Name the blood parasite species.
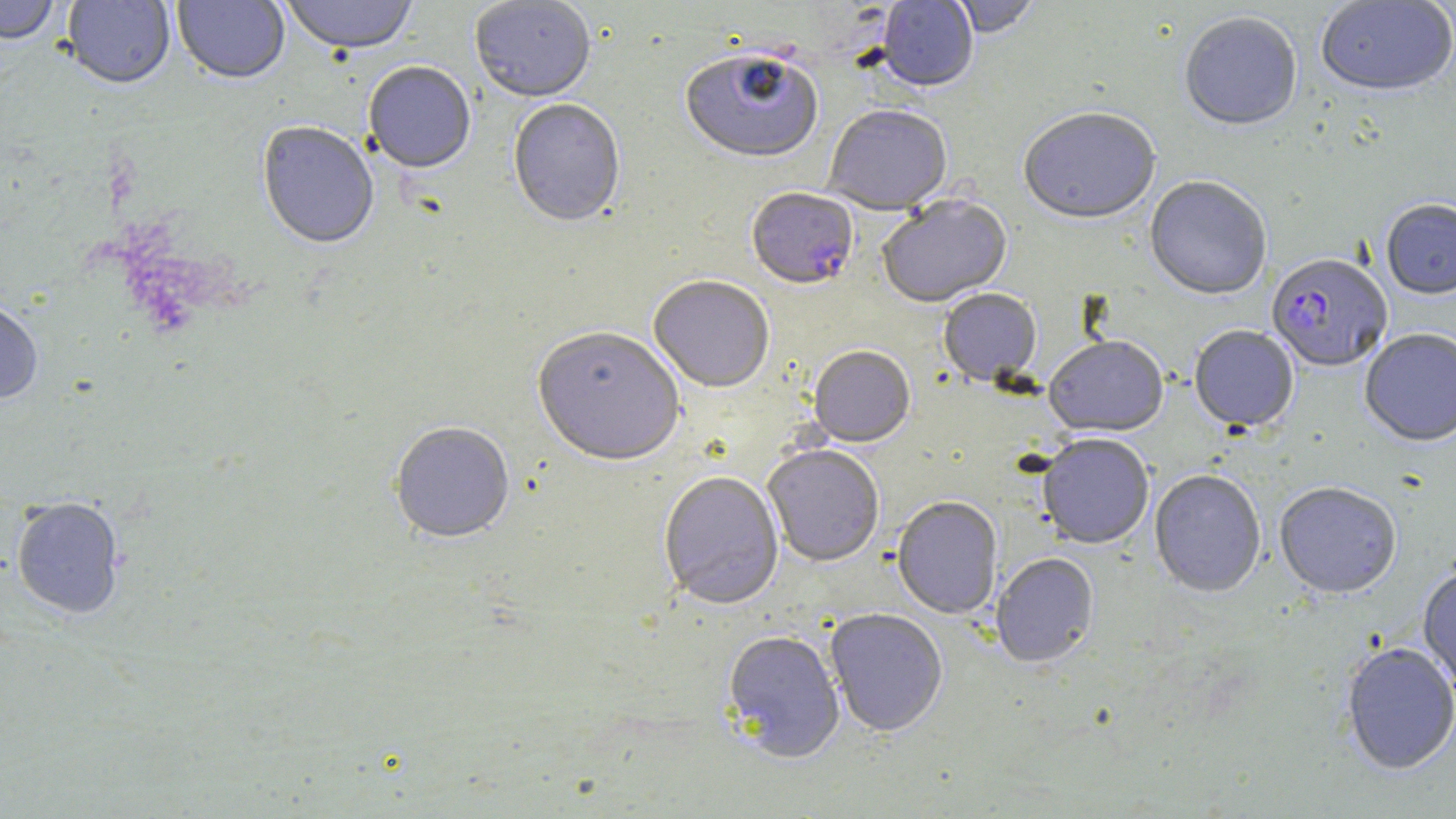

Plasmodium falciparum.

{
  "preparation": "thin blood smear",
  "plasmodium_falciparum_infected_red_blood_cell_locations": "approximate bounding boxes as (x1,y1)-(x2,y2) corner pairs in pixels: (747,190)-(858,293), (1266,254)-(1392,372)",
  "magnification": "1000x",
  "uninfected_red_blood_cell_locations": "approximate bounding boxes as (x1,y1)-(x2,y2) corner pairs in pixels: (0,0)-(60,48), (62,0)-(175,92), (173,0)-(289,87), (279,0)-(418,59), (469,0)-(596,105), (876,0)-(979,94), (948,0)-(1041,40), (1315,1)-(1456,98), (1179,14)-(1302,133), (680,54)-(823,167), (362,63)-(476,177), (508,101)-(626,230), (823,107)-(953,218), (1019,110)-(1161,228), (257,124)-(379,252), (1144,177)-(1272,302), (878,197)-(1013,310), (1380,199)-(1456,299), (648,278)-(774,395), (938,291)-(1042,388), (0,301)-(43,406), (1189,325)-(1299,432), (1359,327)-(1456,446), (532,330)-(685,472), (1044,338)-(1169,438), (809,348)-(915,449), (389,424)-(514,547), (1037,435)-(1154,550), (763,447)-(884,568), (1149,470)-(1266,599), (659,473)-(784,611), (1274,481)-(1402,598), (892,497)-(1003,620), (11,499)-(125,620), (991,555)-(1099,670), (1417,562)-(1456,694), (825,610)-(947,738), (722,633)-(845,766), (1340,641)-(1456,776)",
  "modality": "light microscopy",
  "image_size": "1456×819 pixels",
  "stain": "May-Grünwald-Giemsa",
  "field_of_view": "one of a larger specimen"
}